Give the position of every Plasmodium parasite visible.
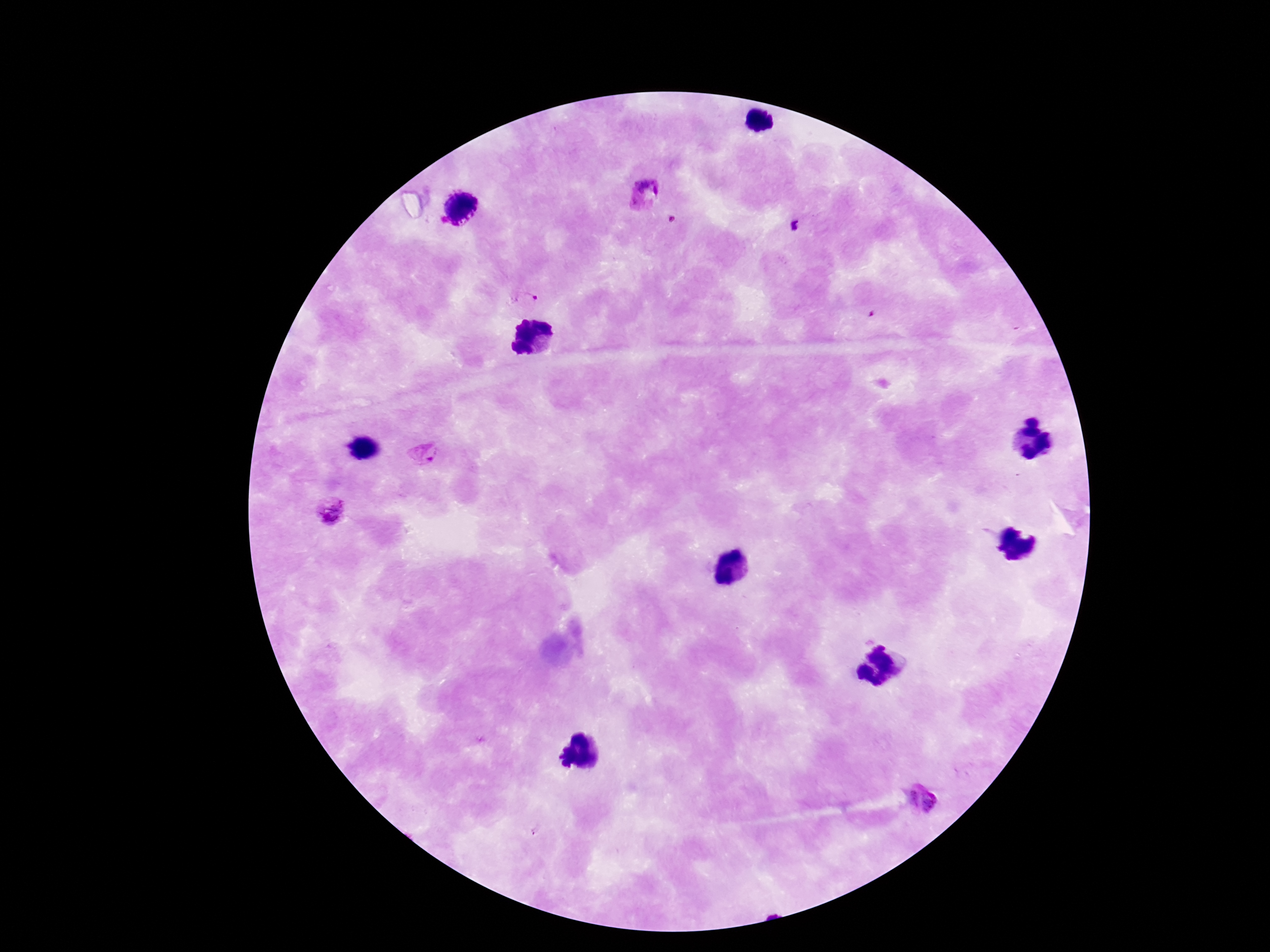
Approximate object centers, in pixels from the top-left corner.
Plasmodium parasites: (x=644, y=192), (x=674, y=220), (x=523, y=301), (x=426, y=456), (x=333, y=512), (x=908, y=799), (x=933, y=801).

Summary:
  - Field of view: one from this slide
  - Preparation: thick blood film
  - Capture: smartphone camera through the microscope eyepiece
  - Stain: Giemsa
  - Magnification: 100x
  - Patient malaria status: positive
  - Image size: 1270×952 pixels